Assess this cell for malaria.
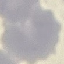

It is uninfected.

Summary:
  - Image type: cell patch, automatically extracted from a larger field of view and resized to 64 × 64 pixels
  - Capture: smartphone camera at the microscope eyepiece
  - Preparation: thin blood film
  - Stain: Giemsa